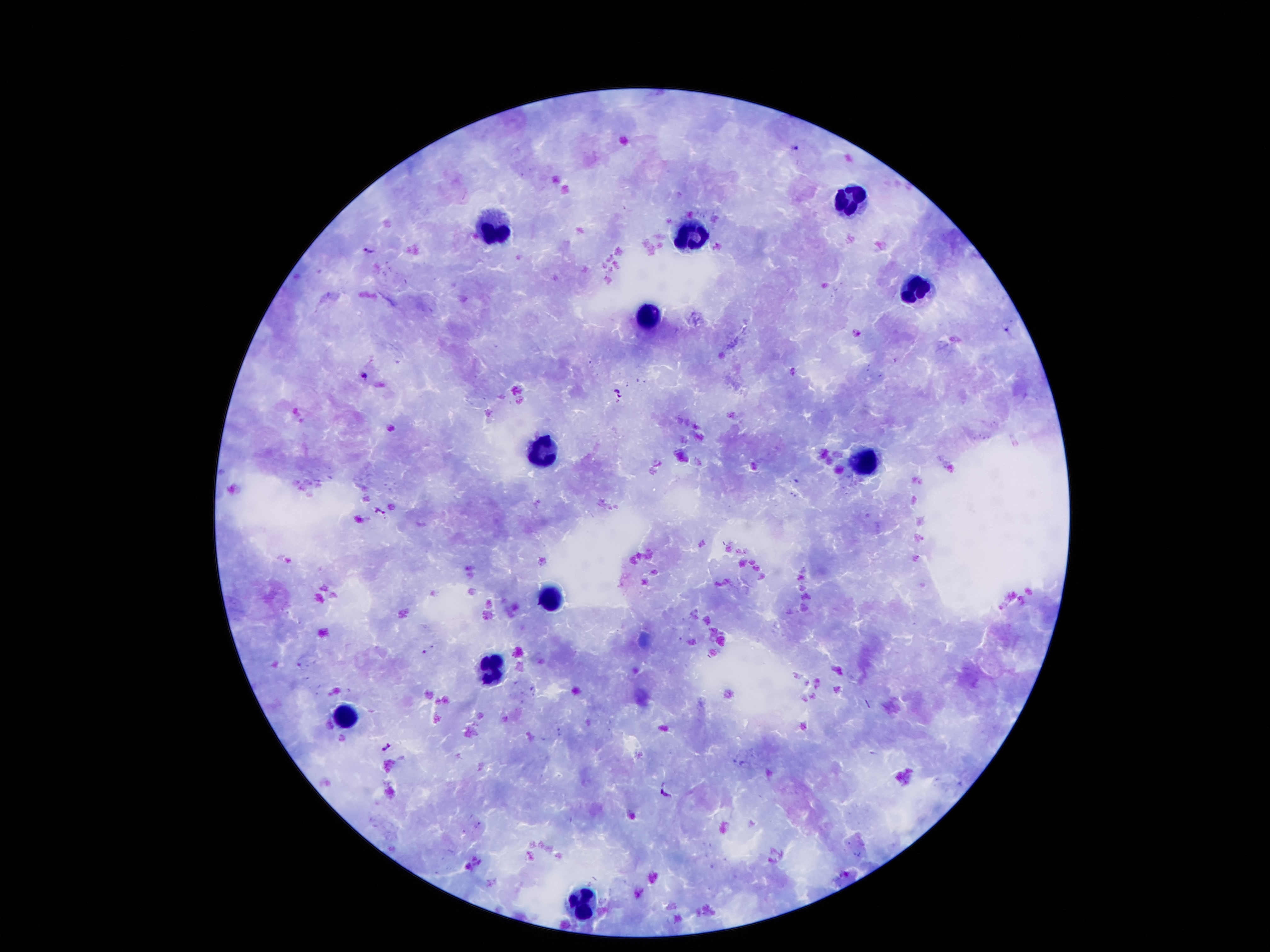

Approximate object centers, in pixels from the top-left corner.
Summary:
  - Leukocyte locations: (x=848, y=203), (x=495, y=226), (x=694, y=234), (x=912, y=296), (x=643, y=324), (x=540, y=455), (x=862, y=458), (x=548, y=598), (x=486, y=671), (x=344, y=721), (x=579, y=906)
  - Malaria parasite locations: (x=793, y=149), (x=370, y=250), (x=364, y=375), (x=619, y=393), (x=378, y=511), (x=386, y=746), (x=665, y=788)
  - Preparation: thick blood film
  - Capture: smartphone camera through the microscope eyepiece
  - Stain: Giemsa
  - Field of view: single
  - Magnification: 100x
  - Patient malaria status: infected with Plasmodium falciparum
  - Image size: 1270×952 pixels